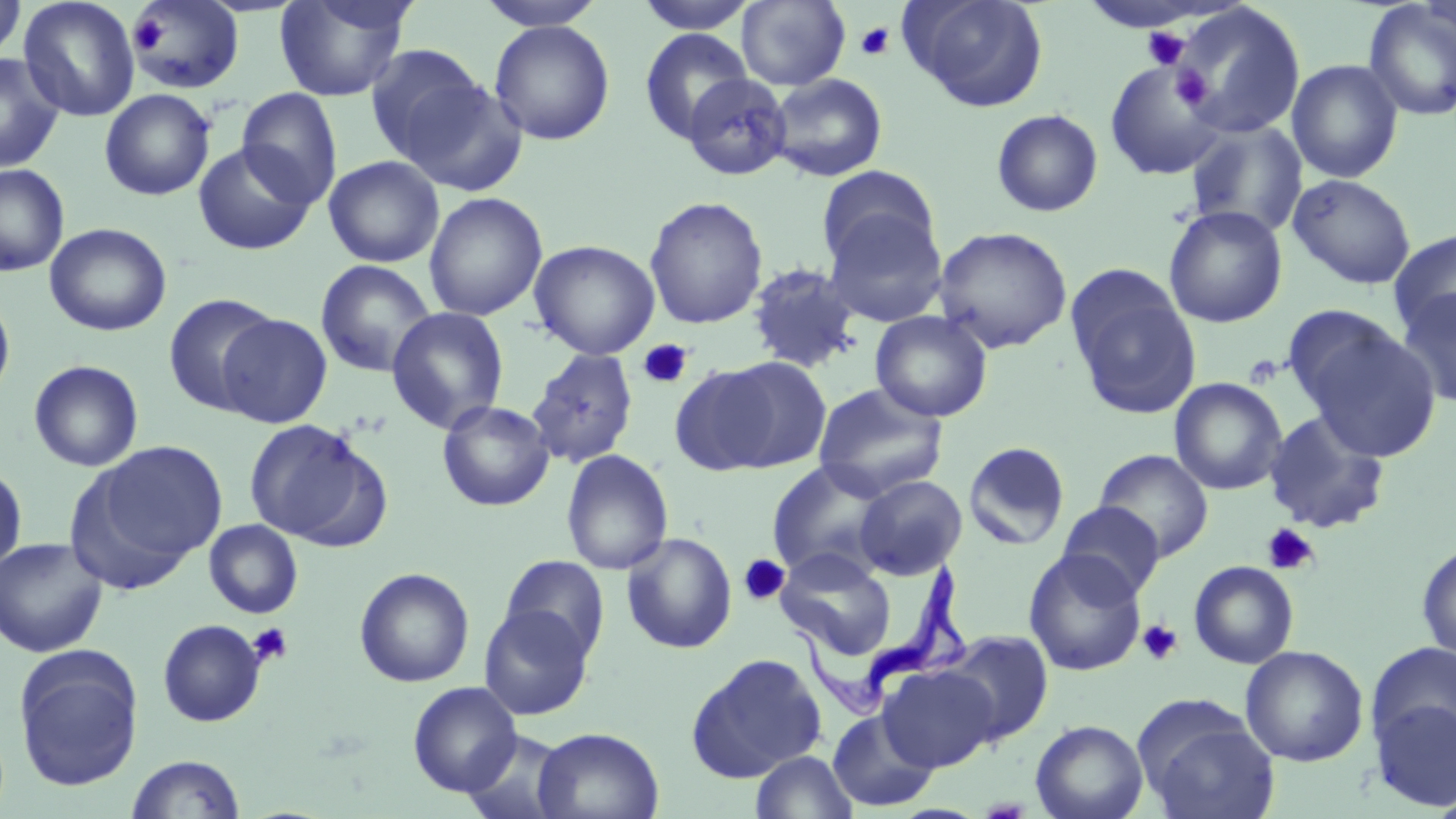
Summary:
  - Coordinate format: approximate bounding boxes as named x1/y1/x2/y2 corners in pixels
  - Platelet locations: (x1=129, y1=17, x2=168, y2=54), (x1=855, y1=22, x2=895, y2=60), (x1=1142, y1=26, x2=1191, y2=70), (x1=1170, y1=54, x2=1229, y2=121), (x1=1172, y1=68, x2=1214, y2=110), (x1=638, y1=339, x2=693, y2=389), (x1=1262, y1=523, x2=1320, y2=575), (x1=737, y1=554, x2=791, y2=607), (x1=1137, y1=620, x2=1183, y2=665), (x1=247, y1=622, x2=293, y2=667)
  - Uninfected red blood cell locations: (x1=0, y1=0, x2=26, y2=64), (x1=18, y1=0, x2=140, y2=122), (x1=273, y1=0, x2=414, y2=103), (x1=475, y1=0, x2=608, y2=30), (x1=633, y1=0, x2=758, y2=34), (x1=901, y1=0, x2=1049, y2=112), (x1=126, y1=1, x2=245, y2=94), (x1=736, y1=1, x2=850, y2=90), (x1=1362, y1=2, x2=1456, y2=123), (x1=1173, y1=3, x2=1306, y2=139), (x1=488, y1=20, x2=615, y2=145), (x1=639, y1=29, x2=754, y2=146), (x1=363, y1=43, x2=488, y2=164), (x1=0, y1=53, x2=65, y2=173), (x1=1104, y1=59, x2=1226, y2=181), (x1=1286, y1=59, x2=1404, y2=183), (x1=767, y1=73, x2=888, y2=182), (x1=681, y1=74, x2=792, y2=180), (x1=398, y1=77, x2=529, y2=198), (x1=236, y1=88, x2=343, y2=208), (x1=99, y1=89, x2=216, y2=200), (x1=991, y1=109, x2=1103, y2=217), (x1=1184, y1=118, x2=1308, y2=238), (x1=193, y1=142, x2=317, y2=255), (x1=323, y1=155, x2=444, y2=268), (x1=0, y1=163, x2=69, y2=276), (x1=816, y1=166, x2=940, y2=274), (x1=1287, y1=173, x2=1416, y2=289), (x1=424, y1=191, x2=547, y2=322), (x1=644, y1=196, x2=768, y2=329), (x1=1163, y1=204, x2=1288, y2=328), (x1=822, y1=209, x2=950, y2=327), (x1=45, y1=222, x2=172, y2=336), (x1=932, y1=226, x2=1073, y2=354), (x1=1388, y1=229, x2=1456, y2=338), (x1=529, y1=240, x2=660, y2=359), (x1=314, y1=259, x2=437, y2=378), (x1=745, y1=262, x2=862, y2=373), (x1=1066, y1=268, x2=1202, y2=419), (x1=1396, y1=287, x2=1456, y2=408), (x1=0, y1=290, x2=16, y2=406), (x1=163, y1=293, x2=281, y2=416), (x1=1280, y1=304, x2=1409, y2=415), (x1=387, y1=306, x2=509, y2=435), (x1=870, y1=310, x2=993, y2=422), (x1=218, y1=313, x2=333, y2=428), (x1=1298, y1=322, x2=1440, y2=460), (x1=527, y1=348, x2=640, y2=468), (x1=711, y1=357, x2=832, y2=472), (x1=28, y1=359, x2=144, y2=472), (x1=668, y1=361, x2=789, y2=475), (x1=1169, y1=377, x2=1287, y2=495), (x1=812, y1=382, x2=949, y2=501), (x1=437, y1=399, x2=555, y2=511), (x1=1263, y1=409, x2=1391, y2=535), (x1=243, y1=418, x2=381, y2=546), (x1=87, y1=441, x2=228, y2=572), (x1=963, y1=441, x2=1070, y2=550), (x1=560, y1=449, x2=673, y2=575), (x1=1094, y1=449, x2=1214, y2=563), (x1=766, y1=461, x2=894, y2=581), (x1=0, y1=462, x2=27, y2=578), (x1=855, y1=475, x2=967, y2=579), (x1=1056, y1=501, x2=1165, y2=601), (x1=204, y1=519, x2=304, y2=619), (x1=621, y1=532, x2=738, y2=654), (x1=0, y1=536, x2=108, y2=657), (x1=1416, y1=541, x2=1456, y2=665), (x1=500, y1=547, x2=736, y2=657), (x1=1023, y1=548, x2=1146, y2=676), (x1=774, y1=549, x2=898, y2=660), (x1=499, y1=555, x2=611, y2=663), (x1=1188, y1=561, x2=1299, y2=669), (x1=354, y1=567, x2=474, y2=687), (x1=478, y1=605, x2=594, y2=721), (x1=157, y1=619, x2=267, y2=727), (x1=941, y1=630, x2=1055, y2=745), (x1=1366, y1=641, x2=1456, y2=752), (x1=1240, y1=645, x2=1369, y2=767), (x1=14, y1=649, x2=143, y2=791), (x1=686, y1=652, x2=828, y2=782), (x1=878, y1=665, x2=1000, y2=772), (x1=407, y1=681, x2=522, y2=797), (x1=1369, y1=697, x2=1456, y2=811), (x1=1133, y1=700, x2=1279, y2=819), (x1=827, y1=709, x2=940, y2=812), (x1=1030, y1=719, x2=1148, y2=819), (x1=533, y1=727, x2=664, y2=819), (x1=461, y1=729, x2=573, y2=819), (x1=749, y1=750, x2=858, y2=819), (x1=125, y1=754, x2=246, y2=818), (x1=1430, y1=789, x2=1456, y2=819)
  - Trypanosoma brucei locations: (x1=791, y1=563, x2=971, y2=723)
  - Slide-level diagnosis: Trypanosoma brucei
  - Modality: optical microscopy
  - Field of view: one of a larger specimen
  - Image size: 1456×819 pixels
  - Stain: May-Grünwald-Giemsa
  - Magnification: 1000x
  - Preparation: thin blood smear